Identify the blood parasite species.
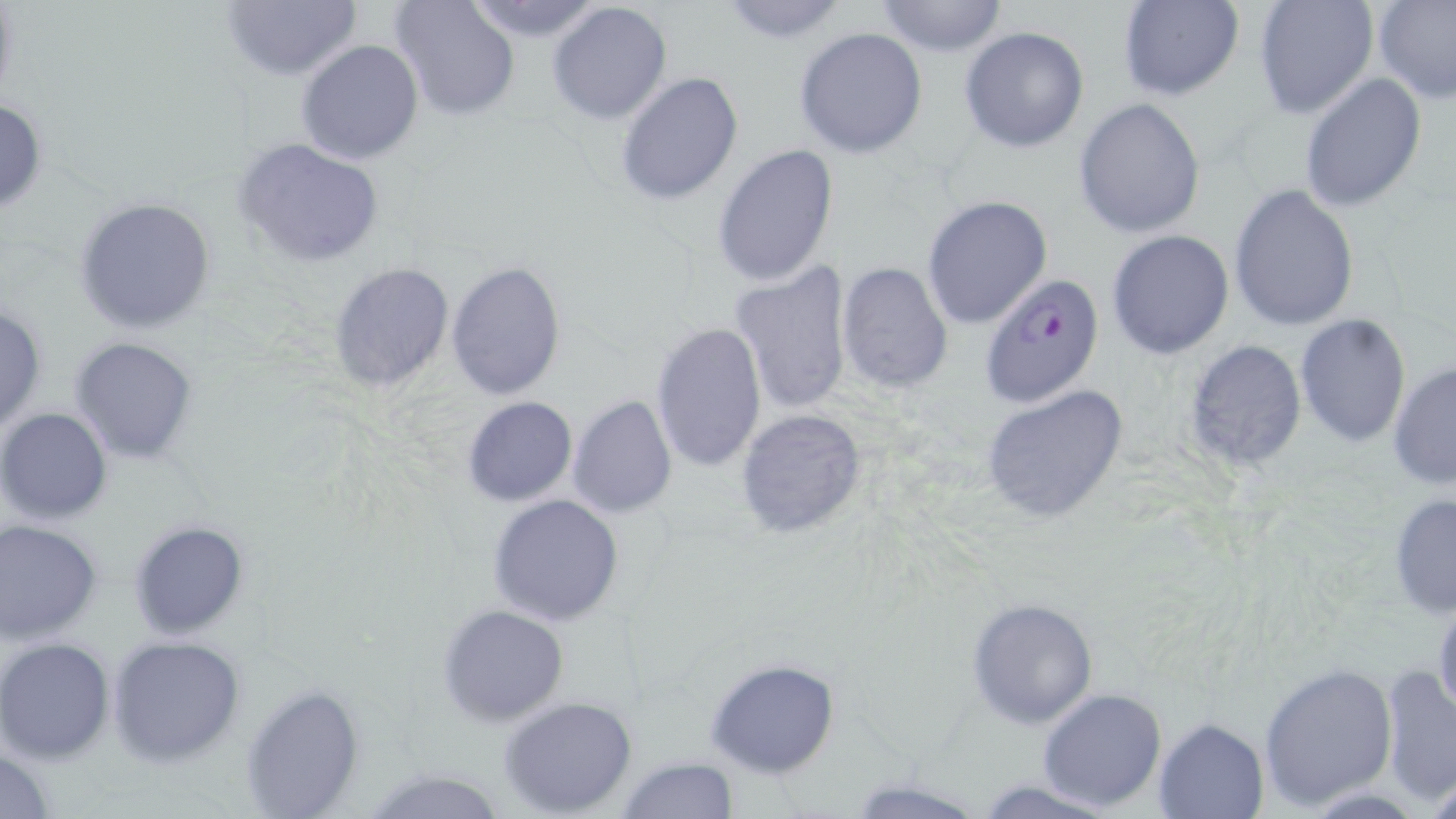

Plasmodium falciparum.

Summary:
  - Coordinate format: approximate bounding boxes as named x1/y1/x2/y2 corners in pixels
  - Plasmodium falciparum-infected red blood cell locations: (x1=982, y1=272, x2=1104, y2=407)
  - Uninfected red blood cell locations: (x1=220, y1=0, x2=362, y2=79), (x1=391, y1=0, x2=519, y2=121), (x1=714, y1=0, x2=853, y2=44), (x1=1119, y1=0, x2=1242, y2=101), (x1=1252, y1=0, x2=1380, y2=120), (x1=1373, y1=0, x2=1456, y2=103), (x1=462, y1=1, x2=608, y2=43), (x1=548, y1=1, x2=672, y2=122), (x1=874, y1=1, x2=1009, y2=56), (x1=959, y1=25, x2=1091, y2=153), (x1=794, y1=27, x2=927, y2=158), (x1=295, y1=40, x2=423, y2=166), (x1=616, y1=73, x2=744, y2=207), (x1=1299, y1=73, x2=1425, y2=214), (x1=0, y1=97, x2=49, y2=216), (x1=1073, y1=98, x2=1206, y2=237), (x1=235, y1=137, x2=386, y2=268), (x1=713, y1=143, x2=841, y2=288), (x1=1229, y1=183, x2=1361, y2=331), (x1=74, y1=195, x2=217, y2=332), (x1=921, y1=195, x2=1052, y2=329), (x1=1106, y1=229, x2=1234, y2=358), (x1=445, y1=260, x2=566, y2=400), (x1=327, y1=261, x2=454, y2=394), (x1=731, y1=261, x2=855, y2=415), (x1=837, y1=262, x2=954, y2=394), (x1=0, y1=302, x2=47, y2=433), (x1=1294, y1=313, x2=1412, y2=447), (x1=650, y1=321, x2=768, y2=475), (x1=70, y1=336, x2=198, y2=465), (x1=1183, y1=340, x2=1307, y2=472), (x1=1387, y1=360, x2=1455, y2=490), (x1=981, y1=385, x2=1133, y2=526), (x1=567, y1=393, x2=677, y2=519), (x1=463, y1=397, x2=577, y2=507), (x1=0, y1=407, x2=113, y2=525), (x1=735, y1=408, x2=869, y2=542), (x1=1388, y1=490, x2=1456, y2=619), (x1=487, y1=494, x2=627, y2=625), (x1=0, y1=518, x2=103, y2=644), (x1=129, y1=519, x2=251, y2=639), (x1=1432, y1=590, x2=1456, y2=724), (x1=968, y1=598, x2=1097, y2=729), (x1=437, y1=604, x2=569, y2=727), (x1=107, y1=636, x2=246, y2=766), (x1=0, y1=637, x2=115, y2=763), (x1=704, y1=658, x2=841, y2=776), (x1=1257, y1=662, x2=1398, y2=810), (x1=1379, y1=662, x2=1456, y2=805), (x1=240, y1=684, x2=366, y2=818), (x1=1038, y1=687, x2=1167, y2=811), (x1=499, y1=696, x2=639, y2=817), (x1=1153, y1=716, x2=1269, y2=817), (x1=1, y1=744, x2=55, y2=818), (x1=614, y1=754, x2=740, y2=819), (x1=363, y1=766, x2=507, y2=819), (x1=972, y1=779, x2=1115, y2=818)
  - Preparation: thin blood film
  - Modality: optical microscopy
  - Field of view: single
  - Image size: 1456×819 pixels
  - Stain: May-Grünwald-Giemsa
  - Magnification: 1000x